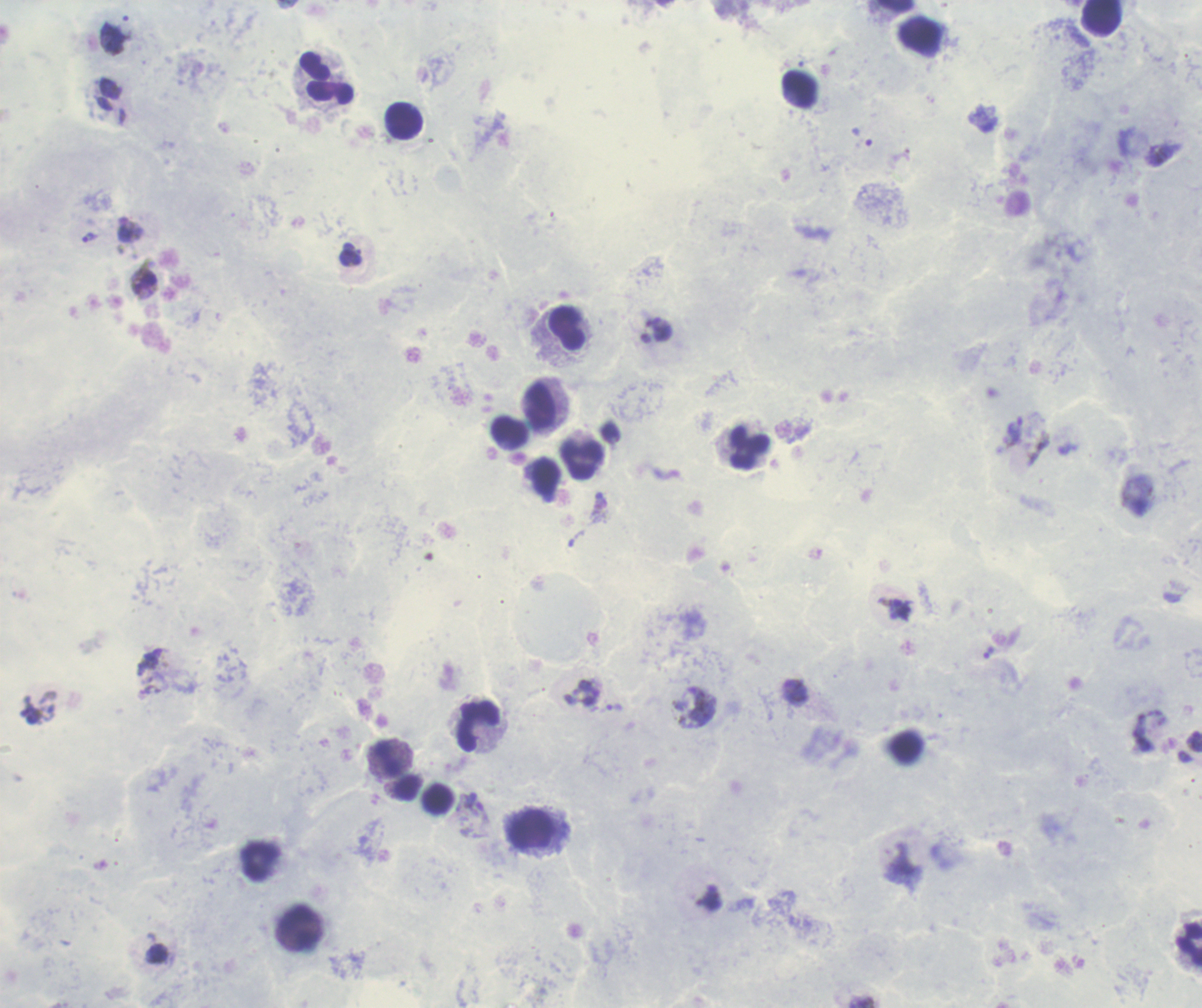
Approximate centers as (x, y) in pixels. Trophozoite locations: (862, 136), (89, 238), (598, 504), (988, 652), (614, 708), (474, 808). Leukocyte locations: (326, 78), (799, 89), (404, 121), (567, 329), (541, 407), (510, 431), (750, 448), (582, 460), (479, 728), (386, 759), (531, 830), (260, 861), (298, 926), (1189, 945). Thick smear of blood. One field from this slide. Background quality: poor. Image is 1202×1008 pixels. Romanowsky stain. Previously used in an actual diagnosis. Result: Plasmodium parasites identified. Coloration quality: good. Captured at 100x magnification.